Classify this cell by malaria status.
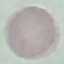

Uninfected.

Giemsa stain. Acquired by smartphone through the microscope eyepiece. Thin blood smear. Cell patch, automatically extracted from a larger field of view and resized to 64 × 64 pixels.